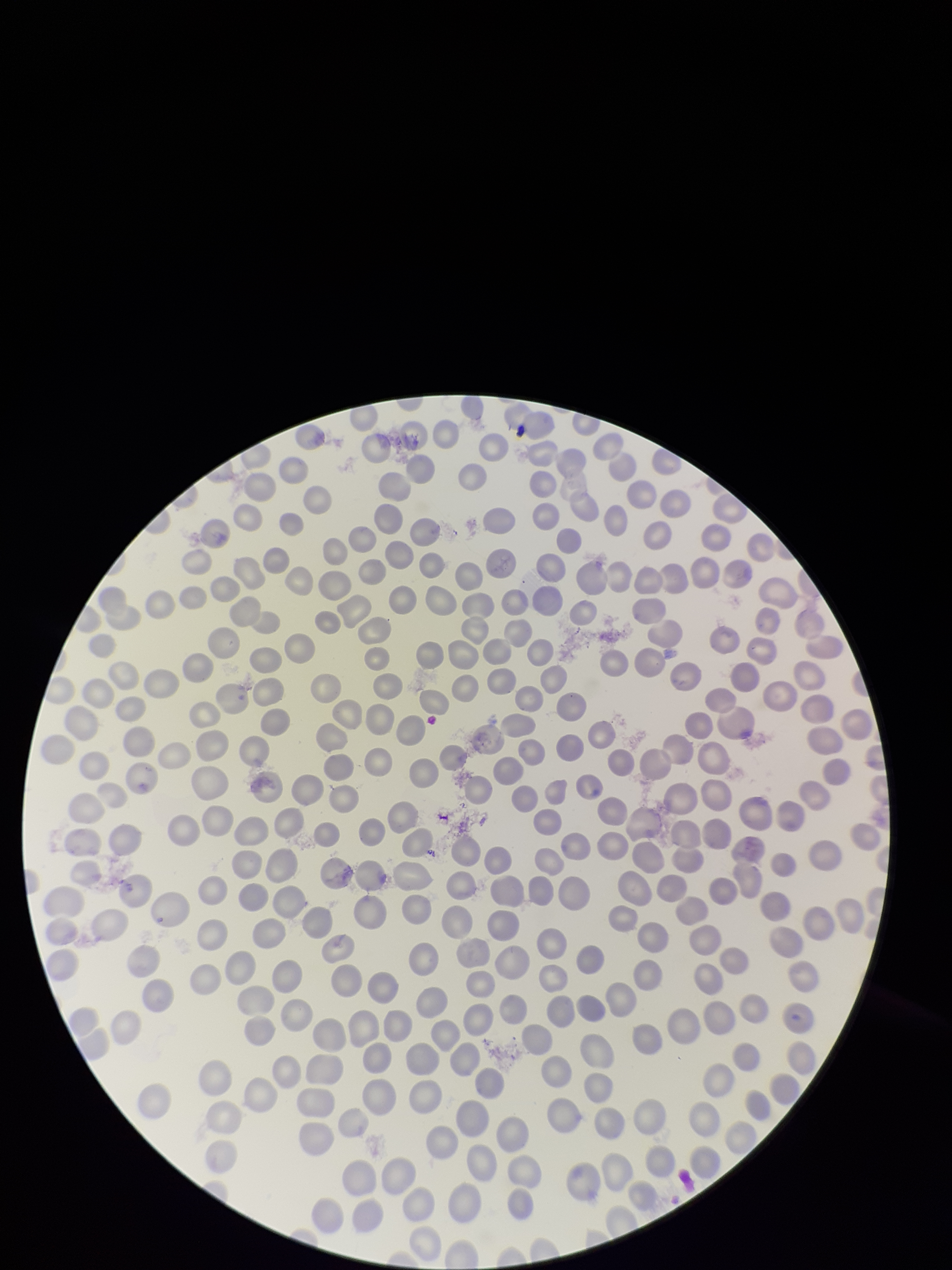
Smartphone photograph taken through the eyepiece of a microscope. Species reported for this patient: Plasmodium falciparum. Parasitized red blood cells: none seen. One field from this slide. Image is 952×1270 pixels. Parasitized red blood cell count: 0. Red blood cell count: 290. Giemsa stain. Patient malaria status: infected. Preparation: thin smear.